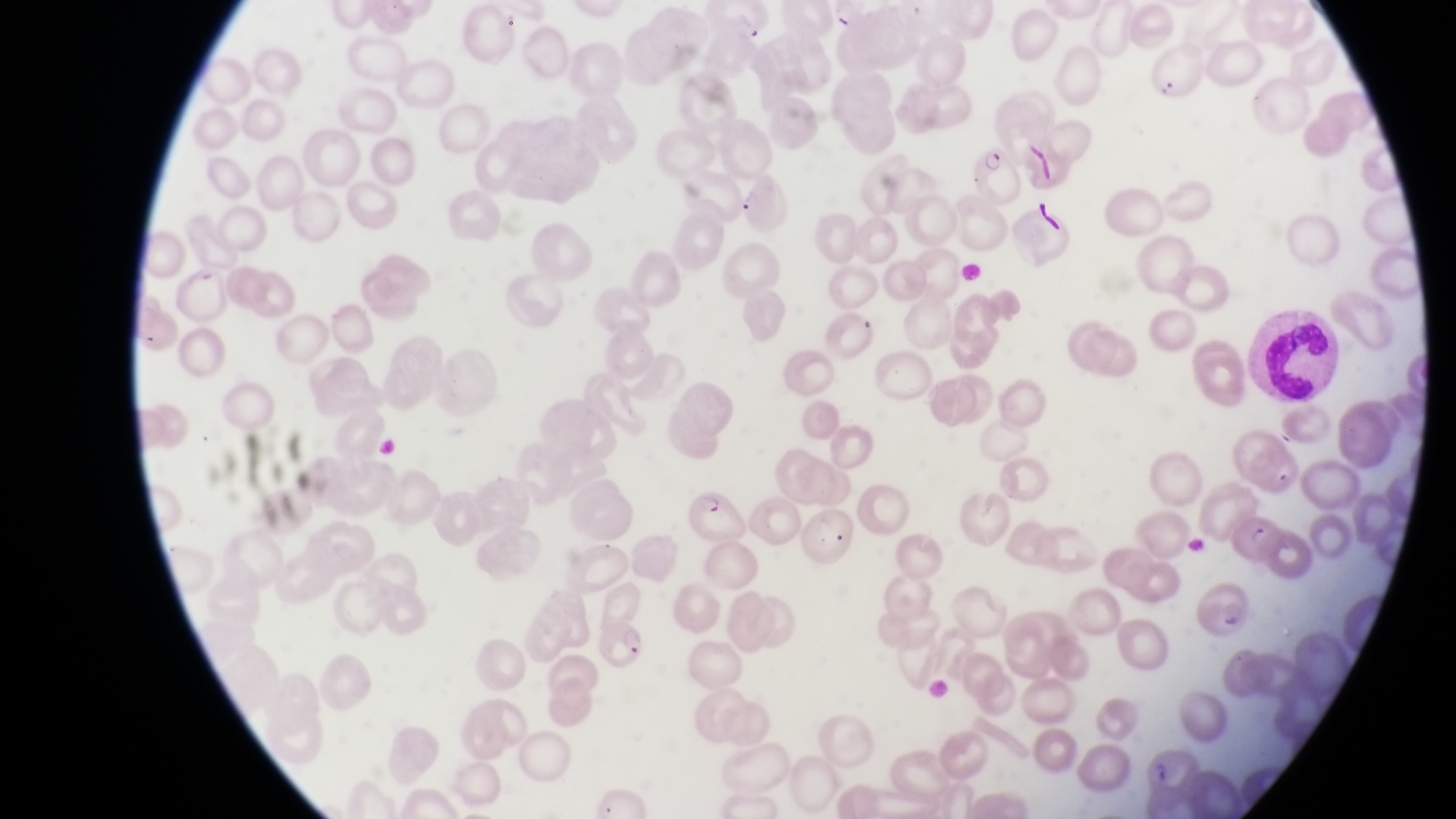

Approximate bounding boxes as [left, top, right, bottom] in pixels.
Summary:
  - Leukocyte locations: [1257, 309, 1339, 402]
  - Parasitised red blood cell locations: [965, 140, 1025, 211], [687, 488, 743, 541], [1231, 512, 1281, 565], [589, 614, 644, 672]
  - Country: Uganda
  - Capture: smartphone photograph through the eyepiece of an Olympus CX-23 microscope
  - Preparation: thin blood smear
  - Field of view: single
  - Image size: 1456×819 pixels
  - Magnification: 1000x